Assess the morphology of the erythrocytes.
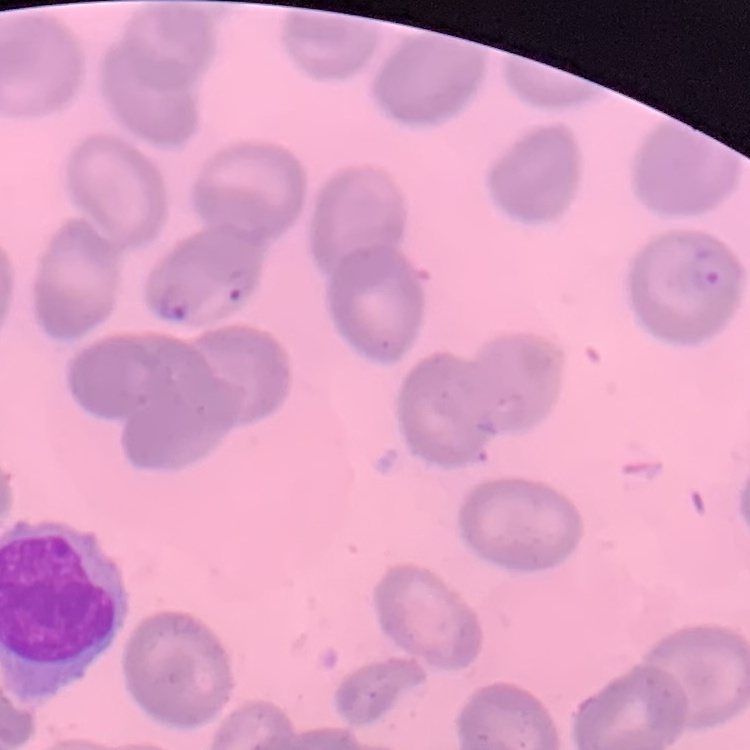
No rouleaux formation.

Summary:
  - Image type: one tile cut from a larger photomicrograph
  - Stain: Field's or Giemsa
  - Preparation: thin blood smear